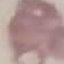

Malaria status: uninfected. Cell patch, automatically extracted from a larger field of view and resized to 64 × 64 pixels. Giemsa stain. Thin blood film. Photographed with a smartphone camera at the microscope eyepiece.